Report the malaria status of this cell.
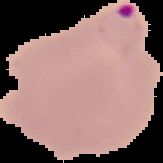
Parasitized.

image_size: 163×163 pixels
image_type: segmented cell region on a black background
preparation: thin blood film